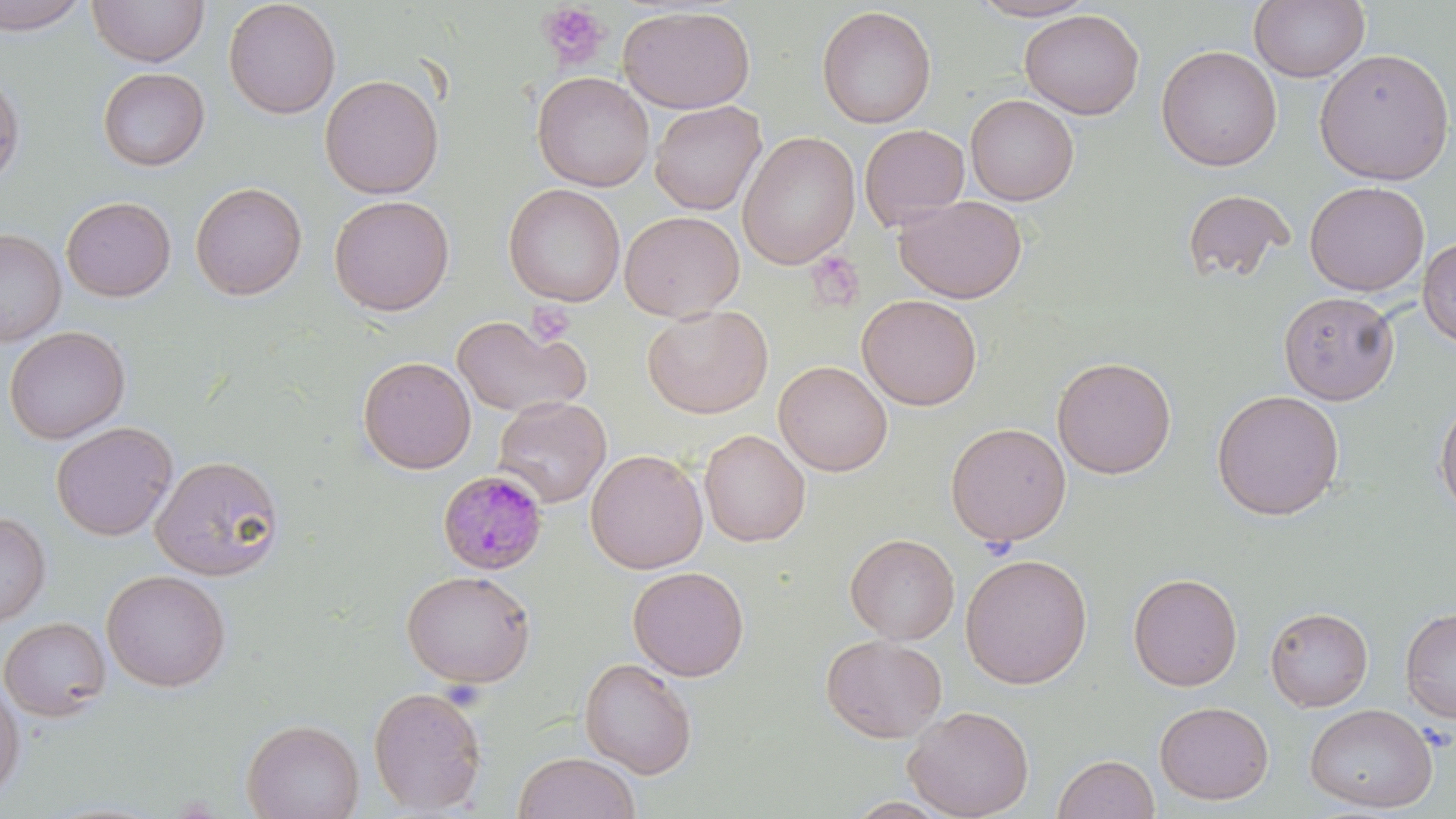

slide-level diagnosis = Plasmodium malariae
magnification = 1000x
modality = optical microscopy
uninfected red blood cell locations = approximate bounding boxes as named x1/y1/x2/y2 corners in pixels: (x1=0, y1=0, x2=91, y2=35), (x1=87, y1=0, x2=210, y2=67), (x1=223, y1=0, x2=341, y2=119), (x1=967, y1=0, x2=1100, y2=22), (x1=1249, y1=0, x2=1369, y2=83), (x1=618, y1=5, x2=756, y2=114), (x1=816, y1=6, x2=937, y2=128), (x1=1019, y1=8, x2=1144, y2=119), (x1=1156, y1=45, x2=1282, y2=172), (x1=1313, y1=47, x2=1455, y2=185), (x1=97, y1=67, x2=210, y2=171), (x1=0, y1=69, x2=26, y2=186), (x1=532, y1=71, x2=654, y2=192), (x1=319, y1=74, x2=444, y2=199), (x1=965, y1=94, x2=1080, y2=206), (x1=649, y1=100, x2=766, y2=215), (x1=859, y1=124, x2=970, y2=230), (x1=738, y1=131, x2=860, y2=270), (x1=1304, y1=181, x2=1429, y2=296), (x1=190, y1=182, x2=308, y2=300), (x1=503, y1=183, x2=625, y2=306), (x1=1180, y1=189, x2=1295, y2=284), (x1=62, y1=193, x2=309, y2=302), (x1=329, y1=195, x2=454, y2=316), (x1=893, y1=195, x2=1028, y2=304), (x1=61, y1=196, x2=176, y2=302), (x1=619, y1=210, x2=744, y2=322), (x1=0, y1=228, x2=66, y2=346), (x1=1417, y1=237, x2=1456, y2=347), (x1=1278, y1=291, x2=1399, y2=404), (x1=857, y1=294, x2=982, y2=410), (x1=642, y1=304, x2=773, y2=418), (x1=452, y1=312, x2=592, y2=418), (x1=4, y1=326, x2=130, y2=444), (x1=1051, y1=355, x2=1177, y2=479), (x1=357, y1=356, x2=476, y2=474), (x1=773, y1=360, x2=892, y2=476), (x1=1211, y1=389, x2=1345, y2=520), (x1=1434, y1=394, x2=1456, y2=520), (x1=493, y1=396, x2=611, y2=508), (x1=51, y1=421, x2=177, y2=541), (x1=945, y1=422, x2=1071, y2=546), (x1=699, y1=428, x2=811, y2=546), (x1=585, y1=449, x2=708, y2=574), (x1=150, y1=455, x2=284, y2=580), (x1=0, y1=512, x2=51, y2=626), (x1=845, y1=533, x2=959, y2=644), (x1=960, y1=553, x2=1093, y2=689), (x1=628, y1=566, x2=749, y2=681), (x1=101, y1=569, x2=231, y2=692), (x1=400, y1=569, x2=537, y2=688), (x1=1127, y1=571, x2=1243, y2=691), (x1=1400, y1=606, x2=1456, y2=723), (x1=1265, y1=607, x2=1373, y2=712), (x1=0, y1=616, x2=111, y2=721), (x1=821, y1=634, x2=947, y2=743), (x1=579, y1=658, x2=698, y2=779), (x1=0, y1=680, x2=26, y2=800), (x1=367, y1=685, x2=487, y2=815), (x1=1154, y1=700, x2=1274, y2=804), (x1=1304, y1=703, x2=1438, y2=813), (x1=903, y1=704, x2=1035, y2=819), (x1=241, y1=717, x2=364, y2=819), (x1=513, y1=752, x2=641, y2=819), (x1=1053, y1=753, x2=1160, y2=819)
preparation = thin blood film
platelet locations = approximate bounding boxes as named x1/y1/x2/y2 corners in pixels: (x1=536, y1=3, x2=610, y2=70), (x1=806, y1=252, x2=864, y2=313), (x1=526, y1=302, x2=575, y2=345)
Plasmodium malariae-infected red blood cell locations = approximate bounding boxes as named x1/y1/x2/y2 corners in pixels: (x1=437, y1=469, x2=548, y2=576)
stain = May-Grünwald-Giemsa
image size = 1456×819 pixels
field of view = one of a larger specimen